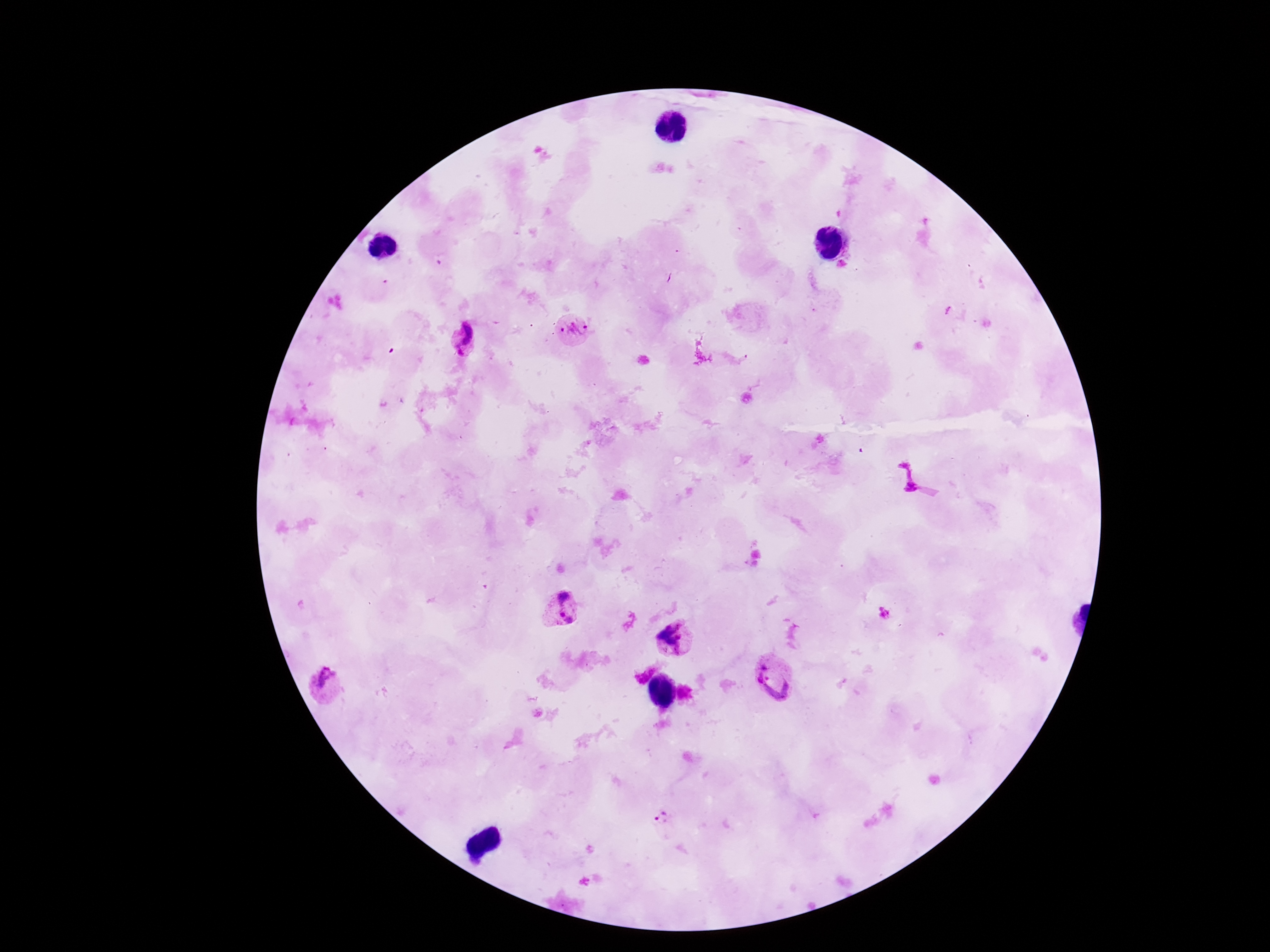
patient malaria status = positive
capture = smartphone camera through the microscope eyepiece
preparation = thick blood smear
image size = 1270×952 pixels
Plasmodium parasite locations = approximate centers as [x, y] in pixels: [572, 331], [462, 339], [908, 474], [559, 609], [675, 639], [777, 677], [323, 686], [663, 819]
stain = Giemsa
magnification = 100x
field of view = single